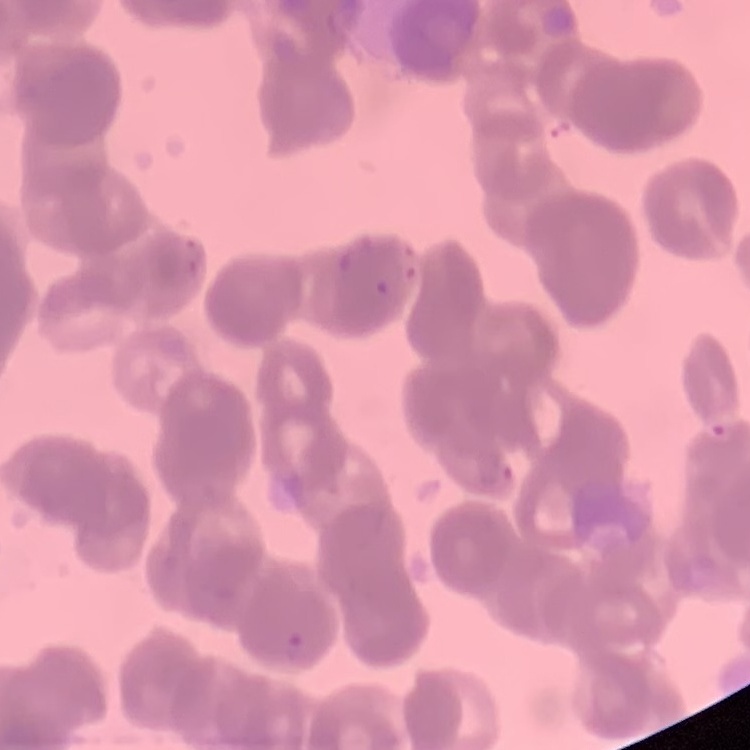

erythrocyte morphology = rouleaux formation
stain = Field's or Giemsa
image type = one tile cut from a larger photomicrograph
preparation = thin blood film